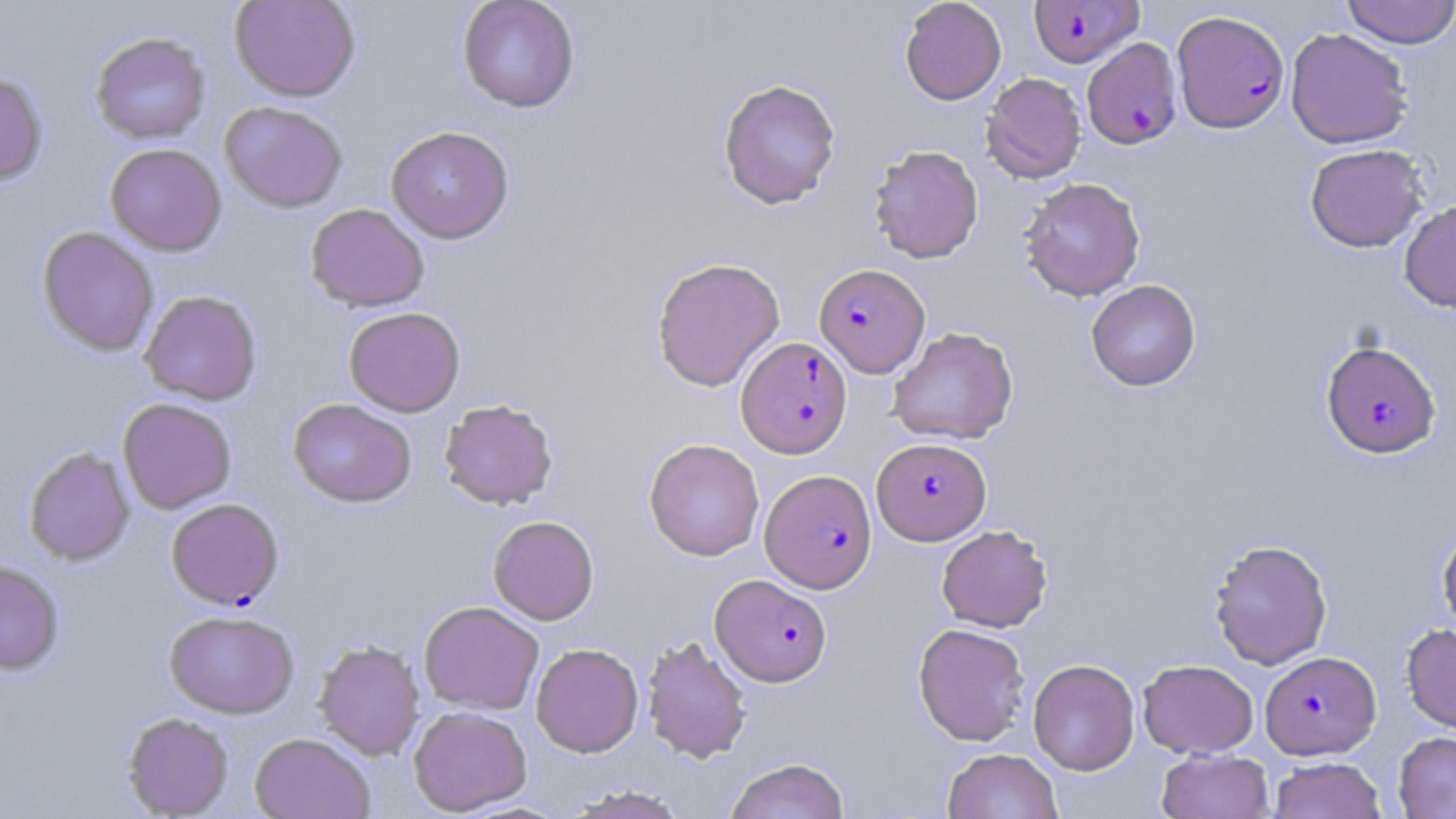
Plasmodium falciparum-infected red blood cell locations = approximate bounding boxes as (x1,y1)-(x2,y2) corner pairs in pixels: (1028,0)-(1145,68), (1172,10)-(1289,133), (1082,38)-(1183,150), (814,263)-(929,377), (736,336)-(853,457), (1320,339)-(1441,459), (872,437)-(991,545), (760,469)-(877,593), (166,497)-(284,609), (710,574)-(832,686), (1260,651)-(1381,759)
slide-level diagnosis = Plasmodium falciparum
modality = optical microscopy
magnification = 1000x
stain = May-Grünwald-Giemsa
image size = 1456×819 pixels
uninfected red blood cell locations = approximate bounding boxes as (x1,y1)-(x2,y2) corner pairs in pixels: (229,0)-(361,102), (457,0)-(580,114), (899,0)-(1006,105), (1341,0)-(1456,48), (1285,27)-(1413,149), (90,31)-(211,144), (0,72)-(49,186), (981,72)-(1086,184), (717,78)-(841,209), (220,101)-(349,213), (385,125)-(515,243), (105,143)-(227,256), (1304,143)-(1429,252), (868,144)-(984,263), (1018,177)-(1146,302), (1399,199)-(1456,313), (305,203)-(430,312), (37,227)-(159,356), (650,257)-(785,391), (1085,279)-(1201,391), (139,290)-(263,406), (344,307)-(465,417), (888,326)-(1018,445), (117,397)-(237,514), (288,398)-(416,507), (439,399)-(559,510), (643,438)-(764,561), (23,447)-(135,565), (488,515)-(599,624), (936,524)-(1052,632), (1437,525)-(1456,639), (1208,538)-(1333,670), (0,560)-(64,675), (419,601)-(544,715), (164,609)-(300,719), (913,622)-(1031,746), (1401,624)-(1456,732), (641,634)-(752,764), (314,639)-(425,760), (530,643)-(644,757), (1028,659)-(1140,774), (1137,659)-(1259,758), (408,706)-(532,815), (122,712)-(233,818), (1393,731)-(1456,818), (250,732)-(375,819), (942,748)-(1064,819), (1157,749)-(1274,819), (725,757)-(850,819), (1269,757)-(1386,819), (562,785)-(692,818)
preparation = thin blood smear
field of view = single